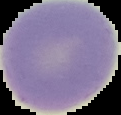
Segmented cell region on a black background. From a thin blood film. Malaria status: uninfected. Image is 121×115 pixels.